State the preparation type.
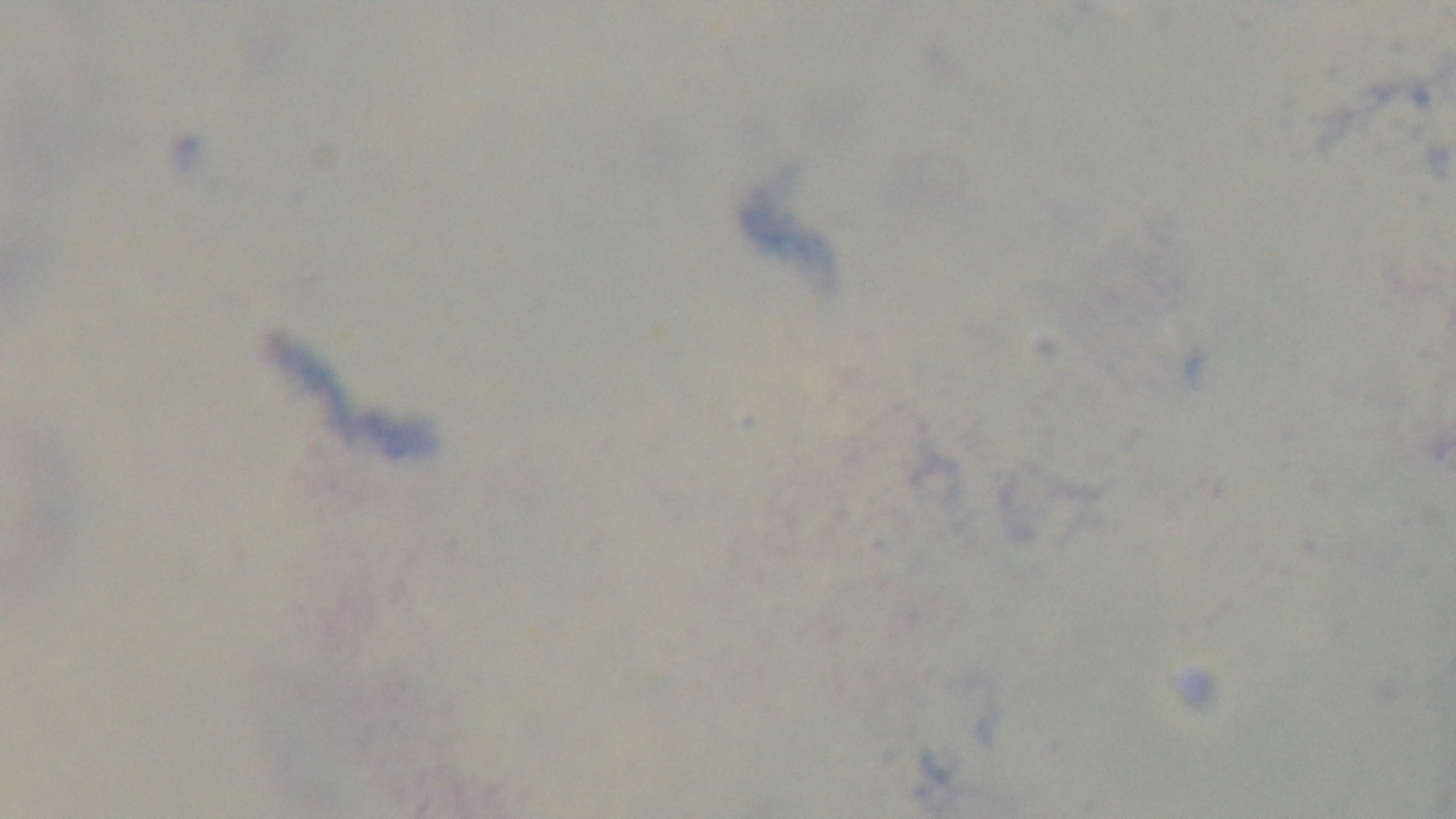

A thick smear.

field_of_view: single
capture: mounted 4K digital camera
malaria_status: uninfected
modality: light microscopy
stain: Giemsa
objective: 100x oil immersion